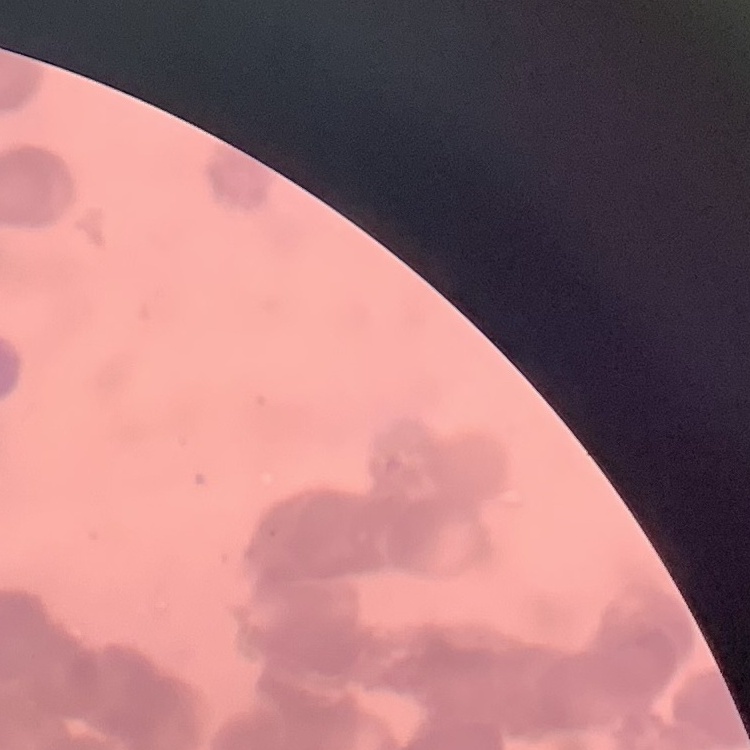
Summary:
  - Red blood cell morphology: rouleaux formation
  - Stain: Field's or Giemsa
  - Preparation: thin blood film
  - Image type: one tile cut from a larger photomicrograph